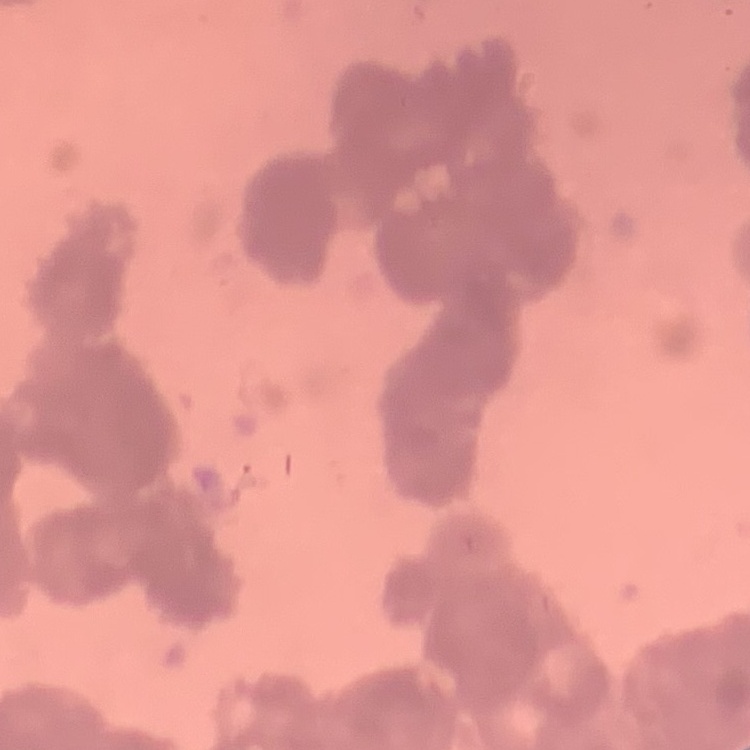
red blood cell morphology = rouleaux formation
preparation = thin blood smear
image type = one tile cut from a larger photomicrograph
stain = Field's or Giemsa